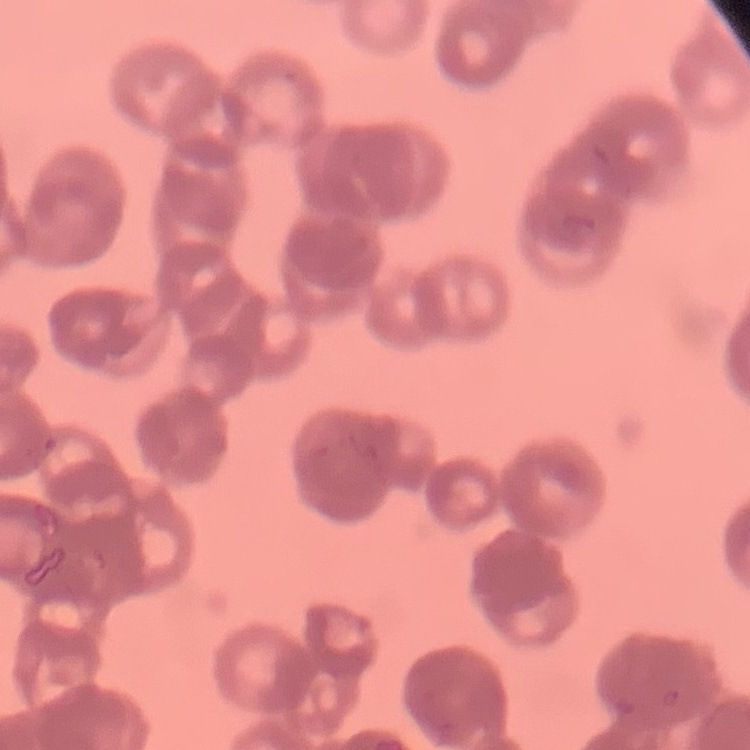
red_blood_cell_morphology: rouleaux formation
image_type: square crop of a larger photomicrograph
stain: Field's or Giemsa
preparation: thin blood film